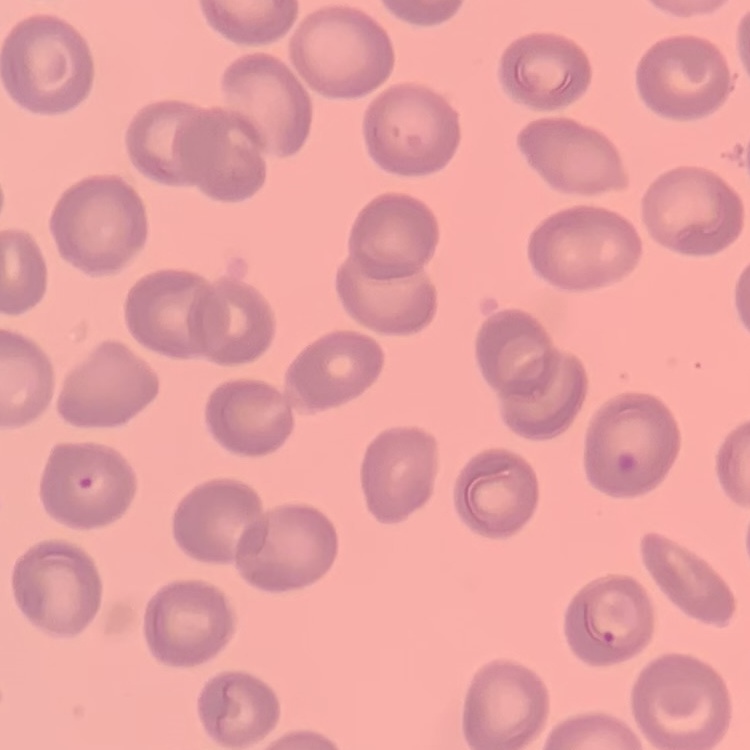
Summary:
  - Red blood cell morphology: no rouleaux formation
  - Stain: Field's or Giemsa
  - Preparation: thin blood smear
  - Image type: one tile cut from a larger photomicrograph